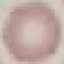

Summary:
  - Malaria status: uninfected
  - Capture: smartphone camera at the microscope eyepiece
  - Stain: Giemsa
  - Image type: automatically extracted cell patch, resized to 64 × 64 pixels
  - Preparation: thin blood film